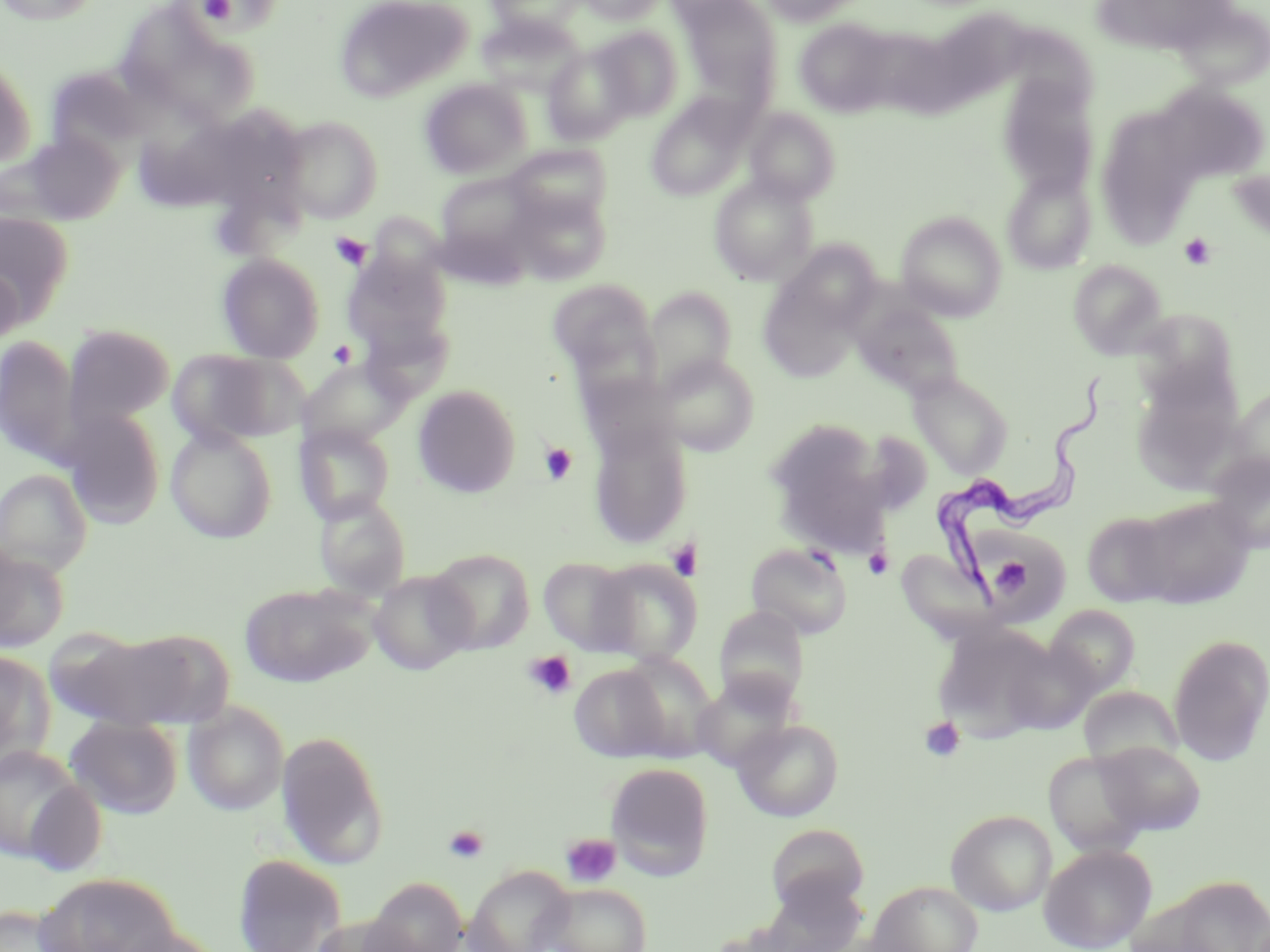
Trypanosoma brucei locations = approximate bounding boxes as (x1,y1)-(x2,y2) corner pairs in pixels: (931,372)-(1108,613)
slide-level diagnosis = Trypanosoma brucei
image size = 1270×952 pixels
stain = May-Grünwald-Giemsa
platelet locations = approximate bounding boxes as (x1,y1)-(x2,y2) corner pairs in pixels: (201,0)-(236,24), (330,232)-(372,271), (1178,233)-(1216,270), (329,340)-(356,368), (539,442)-(577,484), (666,539)-(701,581), (863,548)-(893,580), (991,556)-(1037,600), (522,650)-(577,701), (919,716)-(966,762), (443,824)-(490,863), (560,833)-(622,888)
field of view = one of a larger specimen
modality = optical microscopy
magnification = 1000x
preparation = thin blood smear
uninfected red blood cell locations = approximate bounding boxes as (x1,y1)-(x2,y2) corner pairs in pixels: (0,0)-(103,26), (334,0)-(473,103), (484,0)-(583,36), (578,0)-(665,25), (757,0)-(871,26), (662,1)-(757,27), (681,1)-(783,102), (1176,4)-(1270,91), (119,6)-(223,89), (938,8)-(1036,101), (477,13)-(584,98), (794,18)-(900,117), (592,25)-(683,121), (862,31)-(971,117), (173,44)-(259,127), (542,45)-(637,145), (0,56)-(35,168), (45,67)-(150,162), (996,74)-(1100,196), (420,78)-(531,178), (1152,82)-(1269,184), (646,96)-(752,201), (136,104)-(242,212), (1095,106)-(1202,246), (744,107)-(840,205), (220,109)-(312,224), (280,115)-(383,223), (6,132)-(127,226), (505,143)-(612,226), (1003,170)-(1097,274), (437,172)-(535,257), (709,174)-(818,285), (509,188)-(611,284), (0,211)-(76,326), (896,212)-(1007,321), (777,239)-(881,333), (344,248)-(454,354), (217,252)-(325,362), (1068,260)-(1167,358), (0,265)-(24,353), (758,273)-(866,384), (547,278)-(658,385), (644,286)-(737,389), (852,299)-(966,399), (1132,307)-(1241,408), (63,324)-(175,431), (0,333)-(79,466), (168,348)-(301,447), (656,353)-(760,456), (298,358)-(411,448), (909,372)-(1013,478), (413,385)-(521,498), (1230,386)-(1270,484), (63,409)-(166,529), (763,418)-(884,536), (295,423)-(395,524), (165,427)-(277,543), (589,427)-(692,548), (858,430)-(934,515), (1207,451)-(1270,554), (1,468)-(93,577), (314,494)-(411,599), (1136,495)-(1255,608), (1082,511)-(1178,606), (975,524)-(1070,621), (745,542)-(854,639), (0,548)-(69,652), (427,548)-(535,653), (895,549)-(1000,642), (538,556)-(637,654), (588,559)-(702,665), (369,570)-(475,675), (239,582)-(378,687), (1044,604)-(1141,700), (714,606)-(809,709), (933,621)-(1058,739), (57,629)-(219,731), (1168,633)-(1270,766), (999,637)-(1100,734), (0,649)-(56,775), (613,651)-(720,760), (569,664)-(671,763), (692,672)-(799,771), (1078,686)-(1184,772), (182,701)-(290,815), (65,716)-(183,819), (732,719)-(844,822), (276,730)-(390,871), (1095,740)-(1206,835), (0,743)-(88,863), (1043,750)-(1153,857), (605,761)-(714,879), (22,779)-(107,877), (946,809)-(1057,916), (766,824)-(870,913), (1039,843)-(1157,952), (232,853)-(347,952), (464,865)-(574,952), (36,872)-(179,952), (1137,874)-(1270,952), (364,877)-(468,952), (868,881)-(983,952), (541,883)-(652,952), (0,904)-(80,952), (307,915)-(419,952), (108,927)-(230,952)